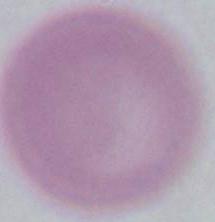

An erythrocyte is shown. 1000x magnification. Micrograph.